Locate every leukocyte (white blood cell).
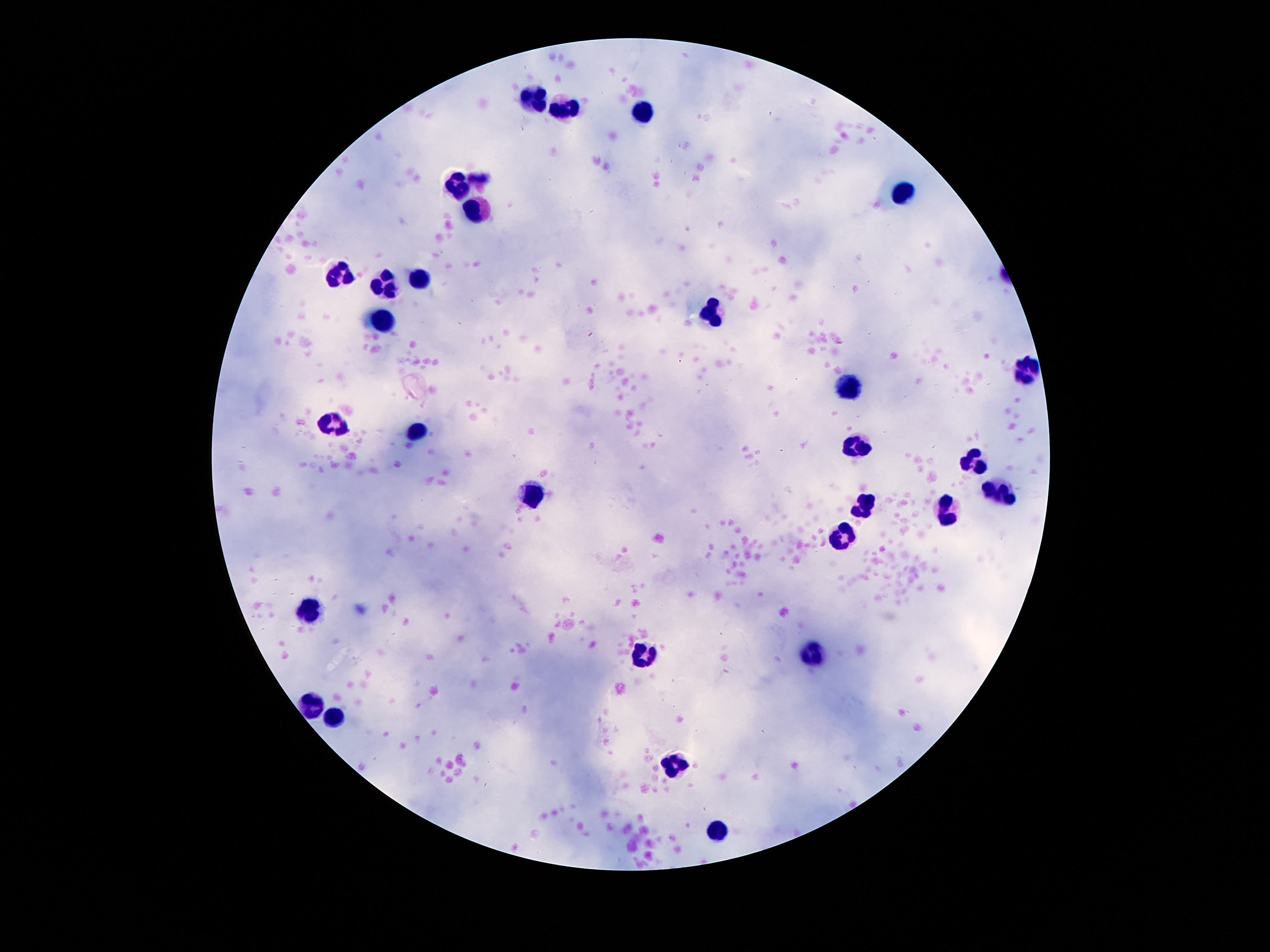
Approximate centers as (x, y) in pixels.
Leukocytes: (533, 94), (568, 106), (643, 115), (457, 178), (902, 194), (475, 213), (338, 273), (417, 282), (380, 285), (708, 315), (382, 320), (1025, 373), (849, 385), (333, 421), (419, 430), (858, 448), (974, 463), (1000, 493), (533, 496), (865, 504), (948, 514), (839, 532), (307, 612), (818, 654), (645, 657), (312, 704), (335, 717), (673, 766), (716, 832).

stain = Giemsa
capture = smartphone camera through the microscope eyepiece
image size = 1270×952 pixels
magnification = 100x
patient malaria status = uninfected
preparation = thick blood smear
field of view = single